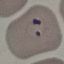
result = malaria parasites detected
preparation = thin blood film
capture = smartphone through the microscope eyepiece
image type = cell patch, automatically extracted from a larger field of view and resized to 64 × 64 pixels
stain = Giemsa